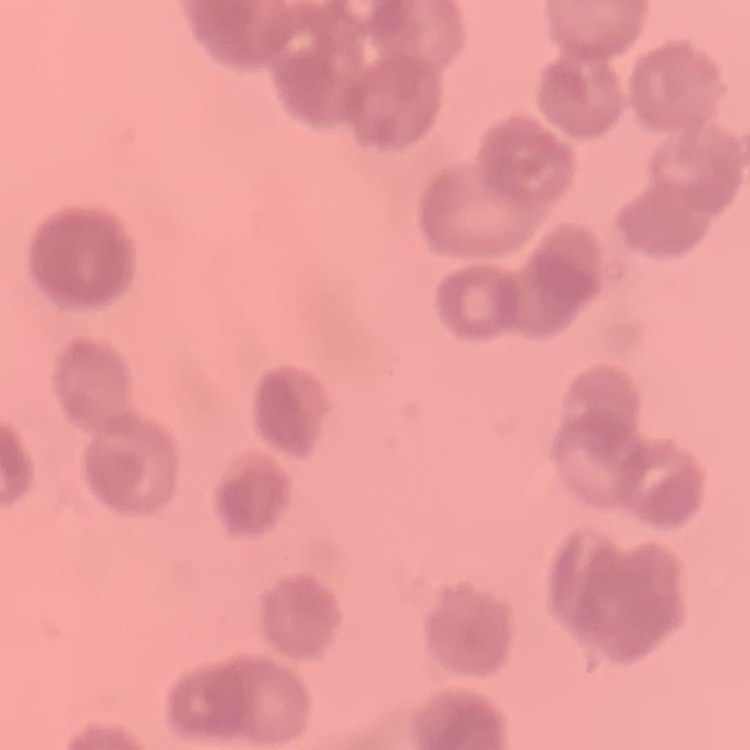

red blood cell morphology = rouleaux formation
image type = one tile cut from a larger photomicrograph
stain = Field's or Giemsa
preparation = thin blood smear